Locate platelets.
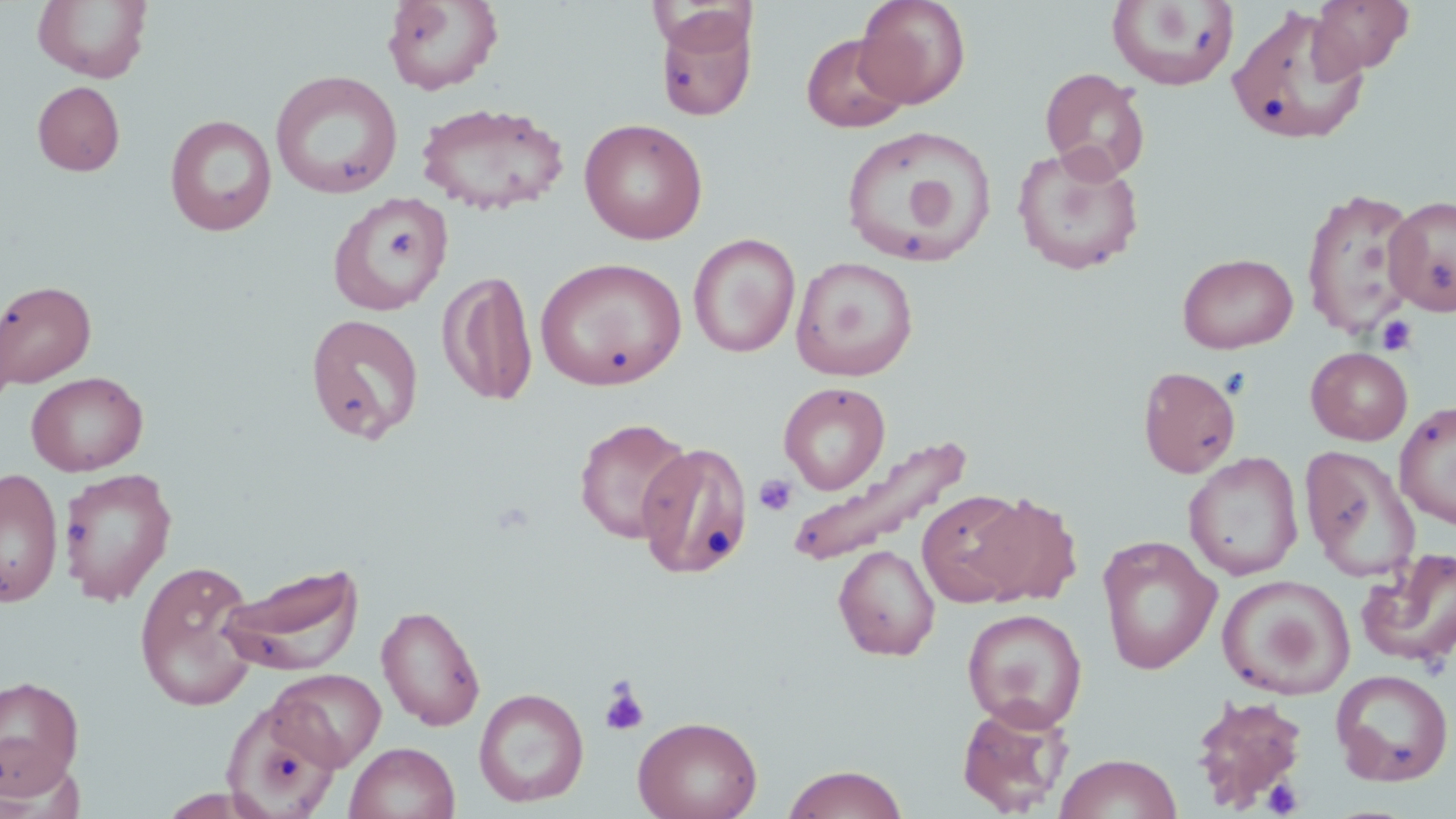

Approximate bounding boxes as (x1, y1, x2, y2) in pixels.
Platelets: (376, 225, 422, 265), (1376, 315, 1418, 355), (754, 474, 797, 516), (598, 682, 648, 736), (1262, 778, 1303, 817).

Summary:
  - Uninfected red blood cell locations: (381, 0, 504, 96), (855, 0, 971, 109), (1107, 0, 1240, 91), (1309, 0, 1415, 77), (32, 1, 153, 83), (1225, 6, 1370, 146), (654, 8, 758, 121), (801, 33, 910, 133), (1040, 67, 1150, 182), (270, 69, 403, 199), (32, 81, 125, 177), (416, 101, 568, 216), (164, 114, 278, 236), (579, 118, 709, 245), (839, 125, 998, 268), (1012, 144, 1145, 275), (1300, 187, 1422, 339), (327, 195, 452, 317), (1384, 195, 1456, 317), (688, 233, 800, 358), (1177, 252, 1298, 354), (535, 256, 687, 390), (790, 256, 918, 381), (438, 270, 539, 407), (0, 280, 96, 387), (304, 313, 425, 444), (1306, 346, 1413, 445), (1138, 366, 1242, 478), (26, 371, 148, 476), (778, 381, 890, 494), (1394, 400, 1456, 529), (574, 417, 692, 544), (785, 432, 970, 568), (635, 440, 755, 579), (1299, 445, 1422, 583), (1183, 452, 1304, 581), (0, 466, 63, 607), (58, 466, 177, 606), (917, 489, 1038, 607), (962, 491, 1083, 607), (1096, 536, 1222, 675), (833, 544, 940, 661), (1356, 547, 1456, 671), (133, 559, 263, 712), (217, 561, 365, 675), (1218, 575, 1356, 700), (376, 604, 486, 731), (961, 608, 1088, 731), (270, 668, 386, 771), (1331, 668, 1454, 786), (0, 674, 85, 798), (474, 687, 589, 808), (1188, 692, 1309, 811), (221, 698, 342, 818), (956, 700, 1075, 817), (633, 715, 762, 819), (345, 741, 460, 819), (1054, 752, 1182, 819), (781, 764, 909, 819)
  - Slide-level diagnosis: no evidence of blood parasites
  - Magnification: 1000x
  - Preparation: thin blood film
  - Stain: May-Grünwald-Giemsa
  - Image size: 1456×819 pixels
  - Modality: light microscopy
  - Field of view: one of a larger specimen